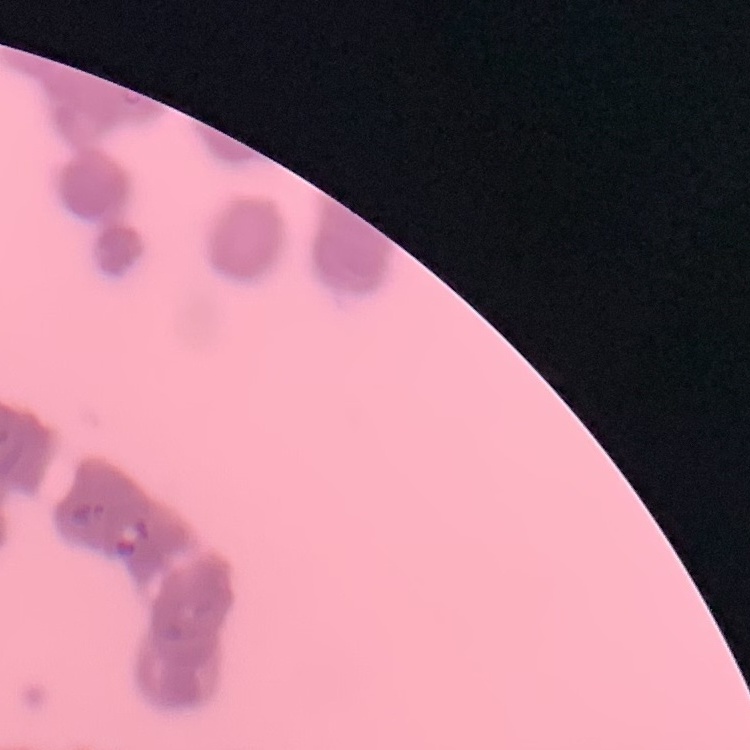 The red blood cells show rouleaux formation. Thin peripheral smear. Field's or Giemsa stain. Square crop of a larger photomicrograph.